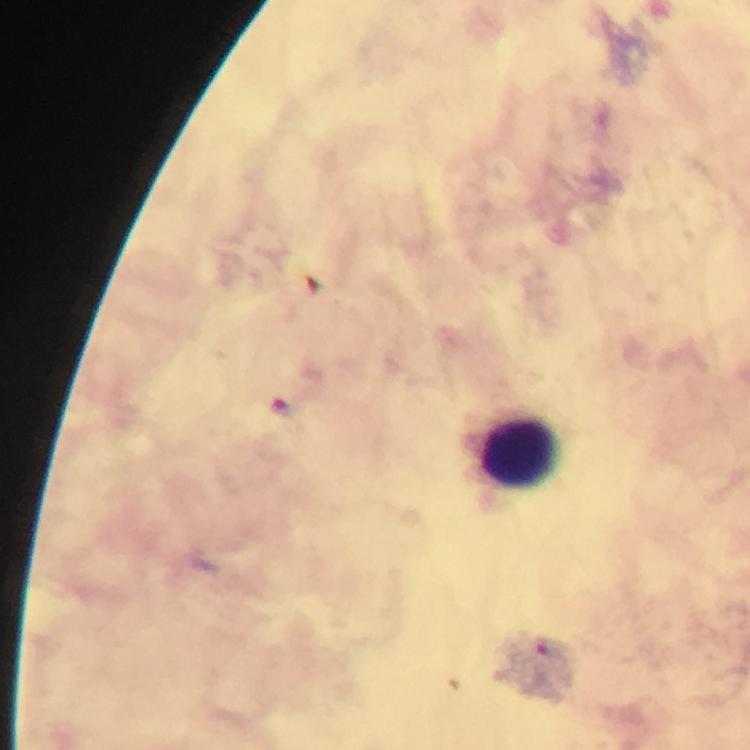
Approximate centers as (x, y) in pixels. Malaria parasite locations: (279, 407). Leukocyte locations: (519, 453). Giemsa-stained preparation. Thick smear. Image is 750×750 pixels. Cropped region of a single field of view. Photographed through the microscope with a smartphone camera. Immersion oil applied. From a malaria diagnostic workup. 100x magnification.